Point out every Plasmodium parasite and every leukocyte.
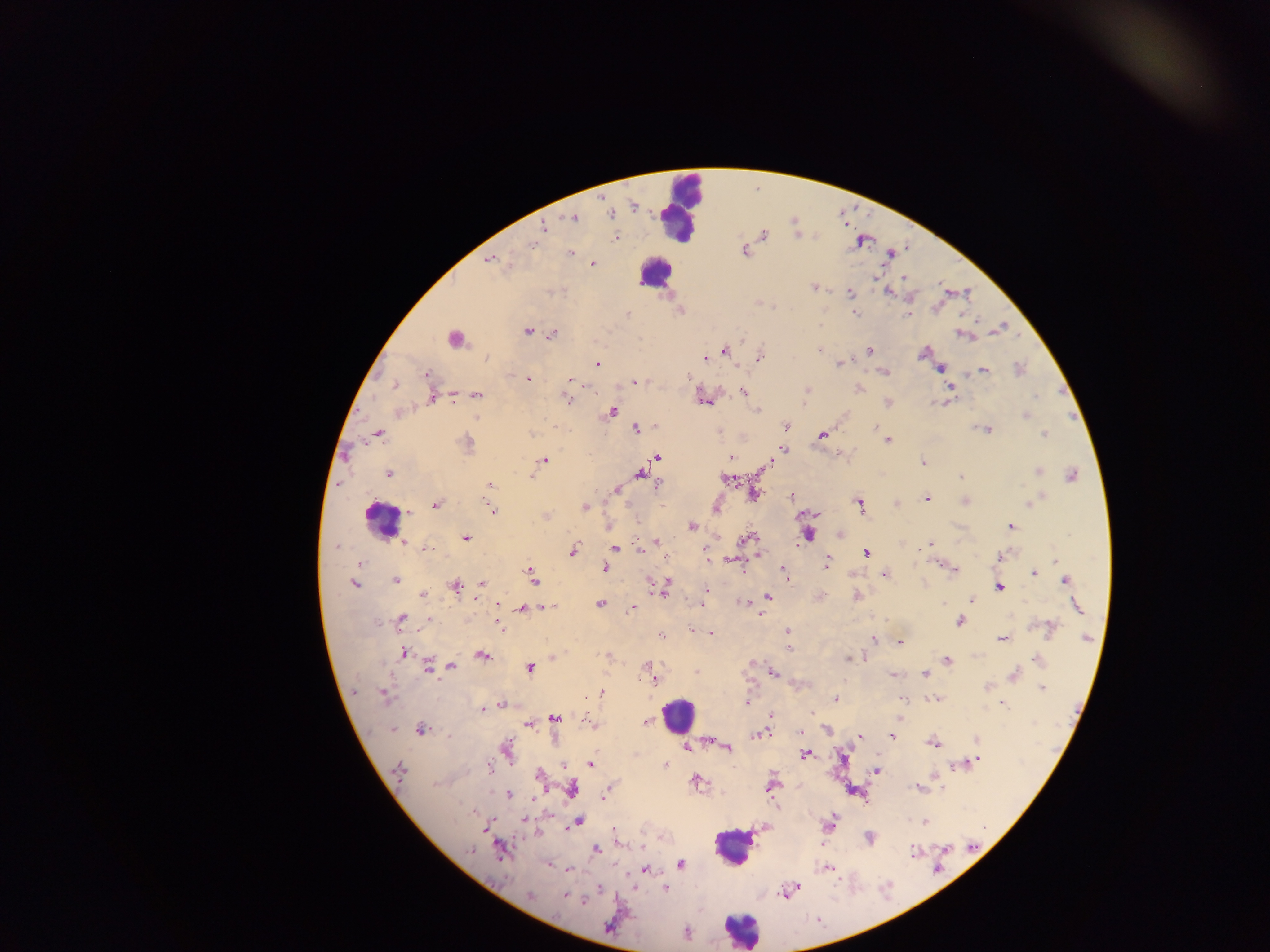
Approximate centers as {x, y} in pixels.
Plasmodium parasites: {633, 207}, {611, 214}, {573, 218}, {544, 227}, {763, 235}, {616, 238}, {532, 245}, {744, 251}, {569, 253}, {489, 260}, {592, 264}, {904, 278}, {814, 287}, {553, 292}, {888, 292}, {850, 293}, {773, 307}, {680, 311}, {854, 313}, {627, 314}, {909, 315}, {1001, 327}, {526, 331}, {553, 334}, {962, 334}, {742, 338}, {820, 349}, {870, 350}, {725, 351}, {923, 353}, {760, 357}, {487, 358}, {705, 358}, {839, 364}, {598, 365}, {941, 368}, {1020, 370}, {983, 371}, {883, 372}, {428, 374}, {688, 377}, {528, 379}, {569, 379}, {635, 382}, {395, 386}, {950, 387}, {859, 389}, {807, 390}, {744, 391}, {476, 395}, {432, 396}, {1034, 396}, {567, 398}, {705, 401}, {935, 402}, {758, 410}, {612, 411}, {400, 413}, {1026, 414}, {786, 425}, {655, 426}, {874, 427}, {636, 429}, {986, 429}, {379, 434}, {822, 435}, {1045, 435}, {888, 440}, {467, 443}, {783, 449}, {657, 457}, {731, 458}, {544, 460}, {922, 463}, {769, 464}, {1037, 471}, {640, 473}, {388, 474}, {531, 476}, {1072, 476}, {961, 477}, {726, 478}, {658, 484}, {490, 485}, {616, 490}, {754, 494}, {792, 497}, {927, 498}, {965, 501}, {1030, 502}, {859, 503}, {896, 504}, {437, 505}, {584, 507}, {716, 508}, {492, 510}, {407, 512}, {545, 516}, {1011, 526}, {692, 527}, {841, 533}, {808, 534}, {465, 538}, {750, 538}, {656, 541}, {405, 543}, {930, 544}, {336, 546}, {616, 547}, {428, 549}, {573, 550}, {640, 550}, {866, 553}, {1003, 556}, {707, 557}, {1055, 561}, {735, 562}, {827, 563}, {360, 564}, {605, 568}, {953, 570}, {784, 573}, {531, 574}, {1034, 574}, {885, 575}, {787, 577}, {396, 580}, {1066, 581}, {666, 583}, {353, 584}, {482, 584}, {455, 587}, {999, 588}, {706, 589}, {663, 590}, {421, 594}, {822, 596}, {857, 596}, {768, 597}, {971, 601}, {743, 602}, {498, 604}, {601, 604}, {943, 604}, {701, 606}, {1076, 606}, {550, 608}, {633, 608}, {521, 609}, {761, 615}, {401, 618}, {428, 620}, {959, 621}, {500, 625}, {692, 629}, {1051, 629}, {788, 632}, {710, 634}, {660, 636}, {1087, 638}, {1002, 639}, {873, 640}, {899, 643}, {789, 649}, {404, 653}, {483, 656}, {553, 657}, {849, 658}, {948, 660}, {1037, 660}, {428, 665}, {450, 666}, {646, 666}, {530, 668}, {696, 672}, {773, 673}, {893, 674}, {925, 674}, {1014, 675}, {653, 679}, {987, 687}, {1042, 688}, {602, 692}, {384, 696}, {586, 696}, {835, 698}, {935, 698}, {747, 703}, {501, 705}, {1003, 705}, {483, 710}, {771, 716}, {554, 718}, {591, 722}, {646, 722}, {528, 724}, {392, 729}, {421, 730}, {827, 730}, {800, 732}, {759, 734}, {859, 736}, {891, 736}, {976, 738}, {710, 741}, {933, 743}, {686, 747}, {727, 747}, {506, 749}, {806, 755}, {979, 759}, {591, 763}, {665, 765}, {489, 766}, {563, 766}, {955, 766}, {399, 770}, {875, 771}, {539, 775}, {696, 781}, {771, 786}, {571, 788}, {918, 788}, {605, 792}, {508, 795}, {524, 820}, {578, 821}, {925, 822}, {830, 824}, {614, 830}, {869, 839}, {596, 849}, {470, 850}, {501, 850}, {914, 851}, {680, 864}, {827, 868}, {569, 870}, {644, 870}, {665, 888}, {788, 890}, {530, 895}, {565, 895}, {583, 900}, {609, 925}, {687, 933}.
Leukocytes: {680, 206}, {655, 272}, {453, 338}, {381, 520}, {679, 714}, {733, 847}, {740, 930}.

Sample from Ghana. Image is 1270×952 pixels. Mobile-phone photograph taken through the microscope. Thick blood film. One field of view.